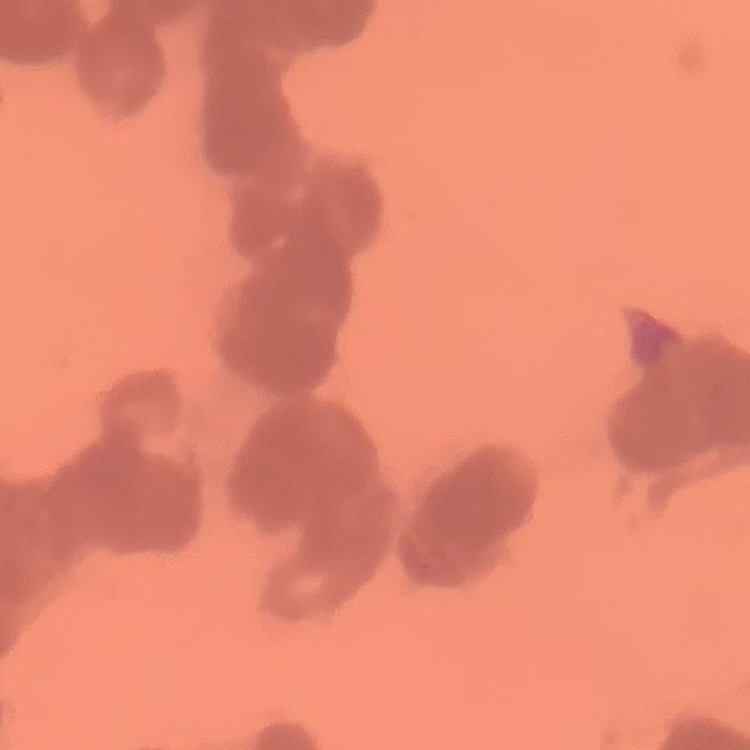
The red blood cells exhibit rouleaux formation. Square crop of a larger photomicrograph. Thin blood smear. Stained with either Field's or Giemsa.